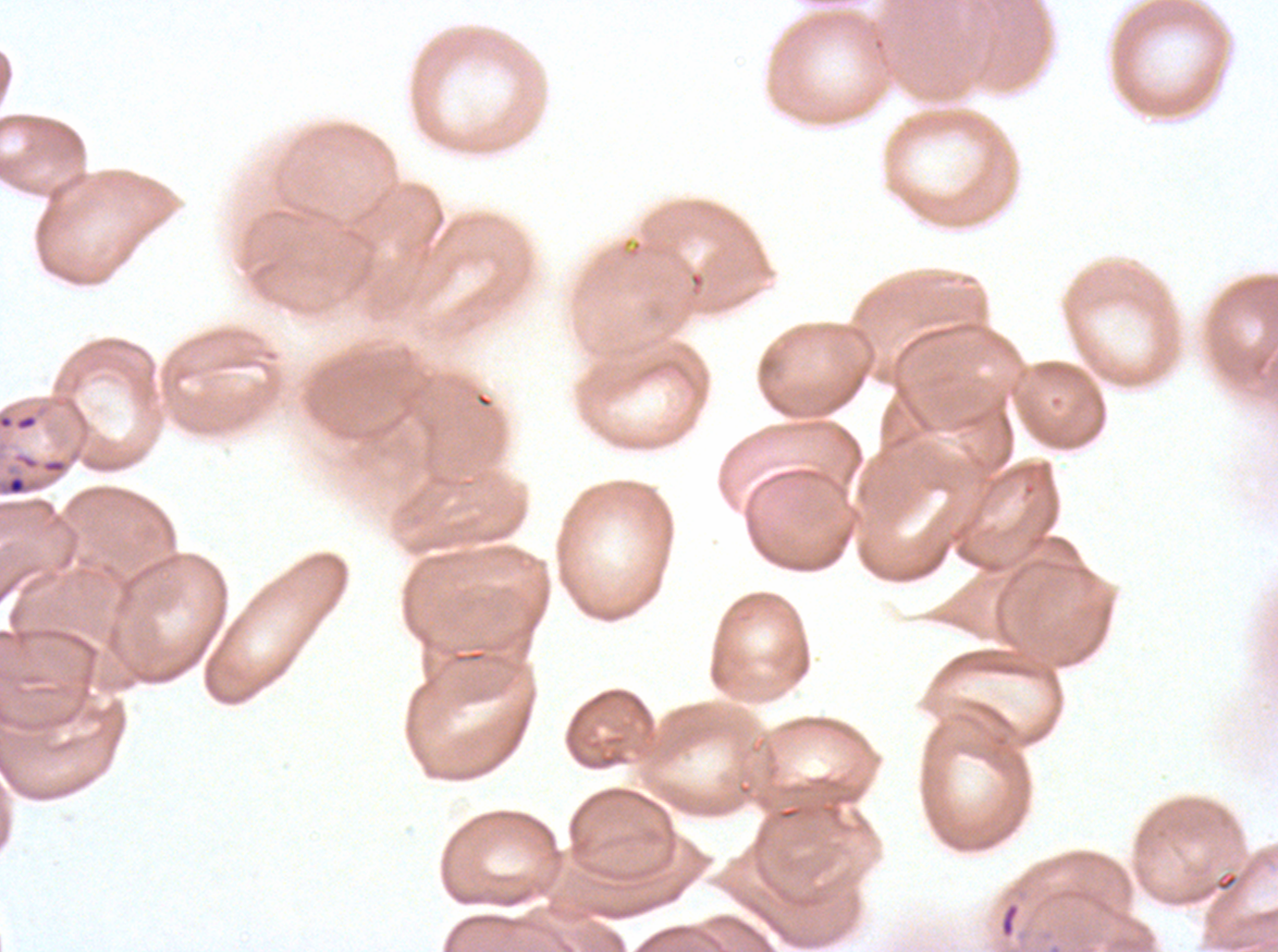

Approximate bounding boxes as (x1, y1, x2, y2) in pixels. Ring locations: (6, 474, 27, 496), (999, 901, 1021, 940). Thin blood smear. Image is 1278×952 pixels. Giemsa stain. One sub-image of a larger composite. P. falciparum cultured ex vivo for 24 to 48 hours, from a patient in The Gambia.